Give the extent of all Plasmodium falciparum-infected red blood cells.
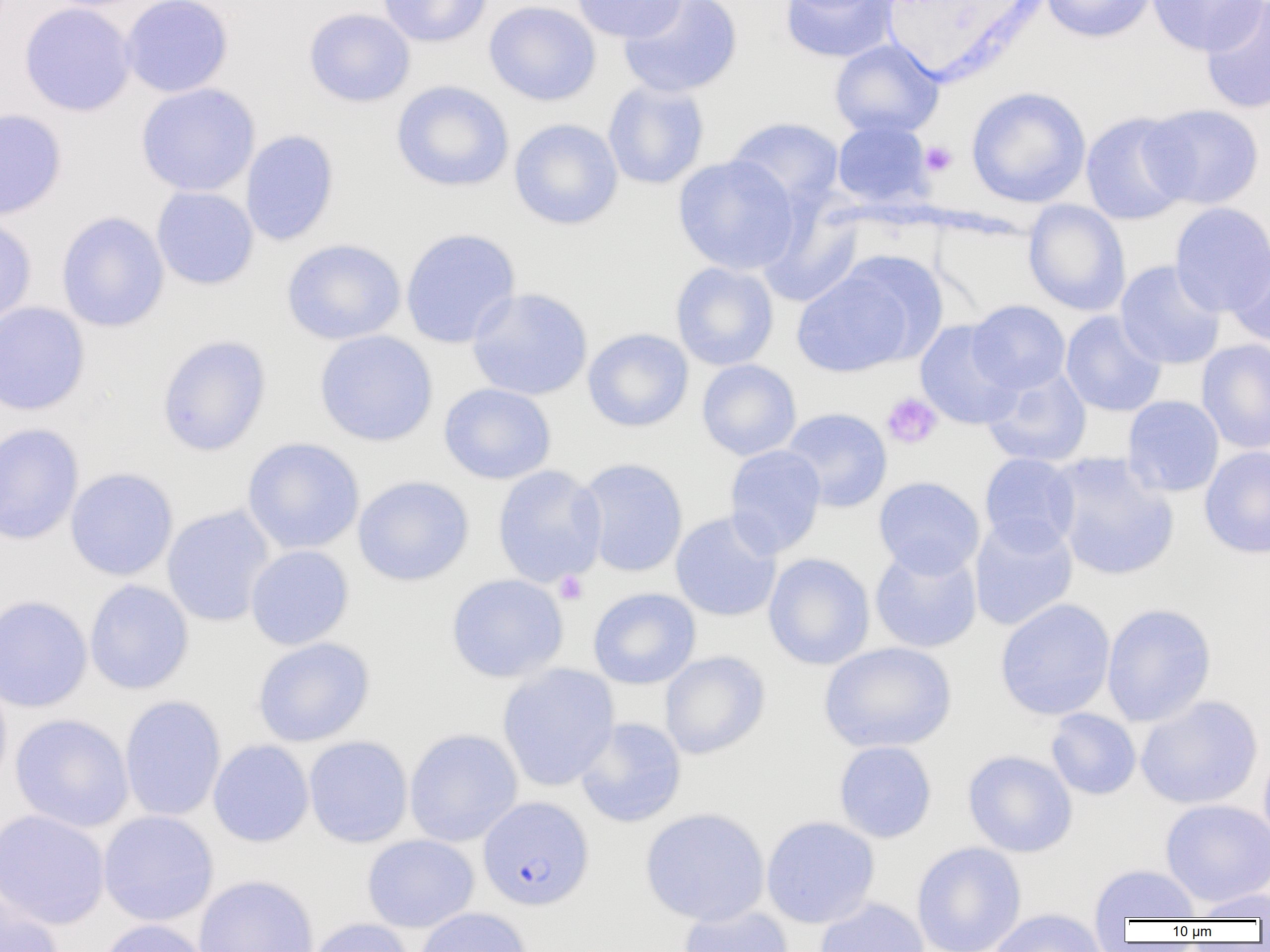

Approximate bounding boxes as [x1, y1, x2, y2] in pixels.
Plasmodium falciparum-infected red blood cells: [477, 796, 594, 911].

Summary:
  - Platelet locations: [920, 141, 957, 177], [881, 392, 942, 449], [554, 571, 588, 605]
  - Uninfected red blood cell locations: [120, 0, 234, 98], [376, 0, 492, 48], [484, 0, 601, 106], [571, 0, 690, 43], [618, 0, 743, 98], [780, 0, 900, 63], [1041, 0, 1156, 43], [1147, 0, 1267, 55], [1200, 1, 1270, 115], [19, 2, 136, 117], [303, 7, 416, 107], [829, 39, 944, 138], [390, 80, 514, 192], [602, 80, 710, 190], [135, 83, 260, 197], [966, 86, 1091, 208], [1140, 104, 1265, 210], [0, 109, 67, 220], [1080, 111, 1192, 226], [726, 116, 845, 212], [509, 118, 623, 230], [832, 120, 934, 208], [240, 130, 340, 246], [672, 155, 800, 274], [151, 186, 259, 290], [1023, 200, 1131, 316], [757, 202, 863, 308], [1169, 202, 1270, 316], [55, 211, 170, 332], [0, 214, 37, 328], [400, 228, 521, 349], [281, 239, 406, 345], [1226, 245, 1270, 349], [791, 260, 925, 378], [1114, 260, 1226, 370], [670, 262, 779, 371], [467, 287, 593, 401], [967, 300, 1070, 394], [0, 301, 90, 416], [1061, 310, 1167, 417], [915, 320, 1023, 430], [583, 328, 694, 432], [314, 330, 438, 447], [156, 334, 272, 457], [1196, 339, 1270, 454], [696, 359, 801, 461], [982, 365, 1092, 467], [438, 382, 556, 484], [1122, 395, 1225, 497], [780, 407, 893, 512], [0, 423, 85, 545], [241, 437, 365, 555], [723, 444, 827, 558], [1199, 445, 1270, 560], [979, 452, 1080, 553], [1047, 453, 1179, 582], [576, 458, 689, 577], [492, 465, 607, 588], [65, 467, 179, 581], [352, 475, 474, 586], [873, 476, 986, 578], [162, 505, 275, 627], [670, 512, 782, 622], [969, 516, 1078, 631], [245, 544, 354, 650], [869, 544, 983, 653], [763, 553, 876, 670], [446, 574, 568, 683], [84, 580, 194, 695], [588, 587, 701, 689], [0, 595, 93, 713], [994, 598, 1116, 720], [1101, 603, 1217, 727], [252, 637, 375, 747], [818, 641, 957, 753], [659, 651, 770, 759], [497, 663, 619, 792], [0, 673, 12, 793], [119, 695, 226, 822], [1135, 695, 1263, 810], [1045, 708, 1141, 800], [9, 713, 134, 832], [574, 717, 687, 828], [403, 728, 523, 847], [303, 735, 413, 848], [208, 740, 314, 847], [833, 740, 937, 843], [1258, 741, 1270, 852], [962, 749, 1078, 857], [1160, 799, 1270, 907], [639, 807, 770, 926], [0, 809, 110, 929], [97, 810, 219, 926], [761, 815, 880, 928], [361, 834, 479, 933], [911, 841, 1027, 952], [1089, 864, 1201, 922], [193, 874, 320, 952], [1190, 887, 1270, 921], [0, 892, 65, 952], [814, 897, 929, 952], [678, 904, 794, 952], [414, 906, 533, 952], [987, 908, 1109, 952], [95, 918, 212, 952], [305, 918, 414, 952]
  - Slide-level diagnosis: Plasmodium falciparum
  - Image size: 1270×952 pixels
  - Magnification: 1000x
  - Modality: optical microscopy
  - Field of view: single
  - Preparation: thin blood film